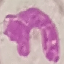

Malaria status: uninfected. Cell patch, automatically extracted from a larger field of view and resized to 64 × 64 pixels. Thin blood smear. Giemsa stain. Photographed with a smartphone camera at the microscope eyepiece.